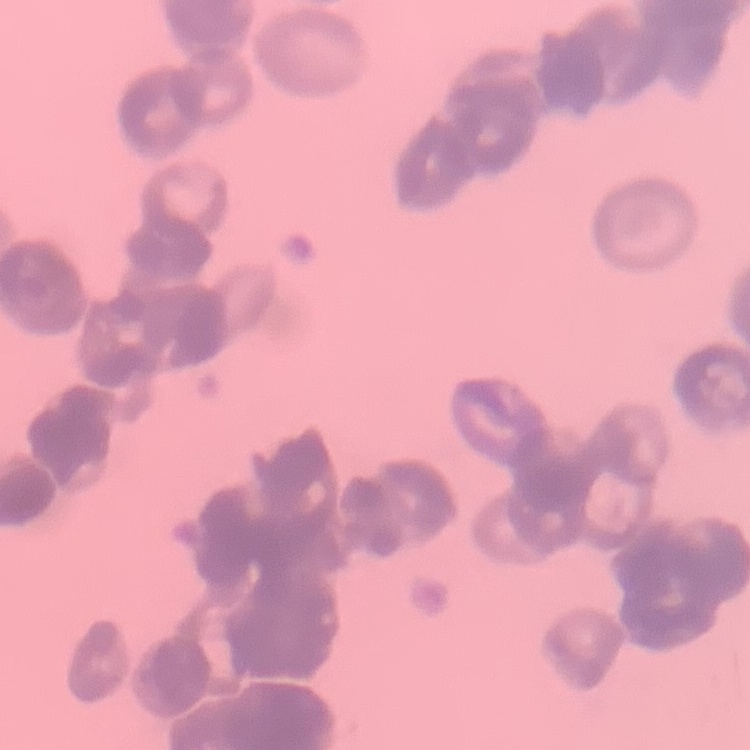
The red blood cells show rouleaux formation. Stained with either Field's or Giemsa. Thin blood film. Square crop of a larger photomicrograph.